Locate and identify every blood parasite.
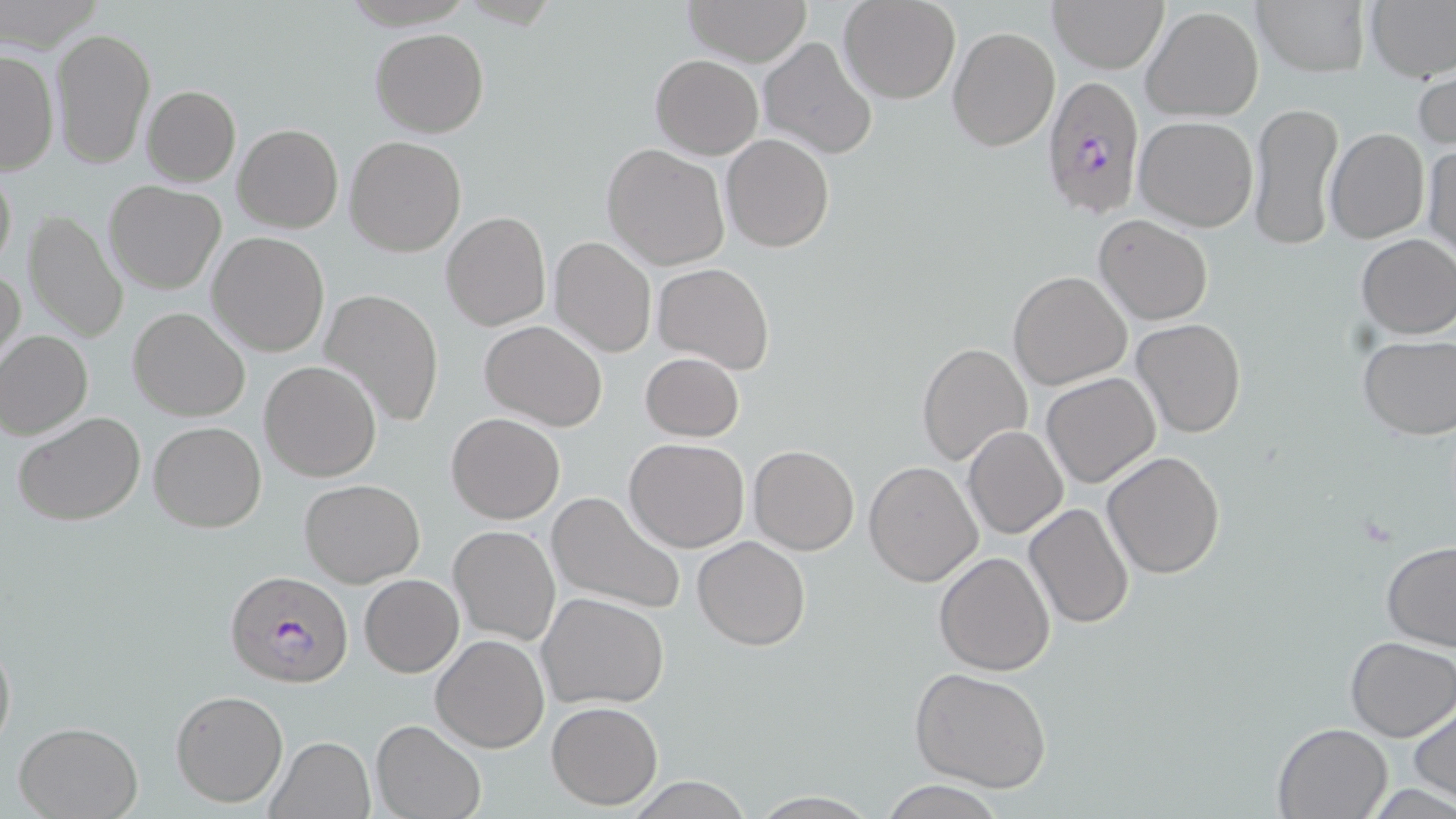

Approximate bounding boxes as named x1/y1/x2/y2 corners in pixels.
Plasmodium falciparum-infected red blood cells: (x1=1039, y1=74, x2=1146, y2=221), (x1=224, y1=568, x2=353, y2=691).
No Plasmodium ovale, Plasmodium malariae, Plasmodium vivax, Babesia divergens, or Trypanosoma brucei observed.

Uninfected red blood cell locations: (x1=3, y1=0, x2=105, y2=52), (x1=684, y1=0, x2=811, y2=65), (x1=838, y1=0, x2=961, y2=103), (x1=1048, y1=0, x2=1168, y2=72), (x1=1250, y1=0, x2=1371, y2=76), (x1=1365, y1=0, x2=1455, y2=81), (x1=1141, y1=5, x2=1264, y2=122), (x1=51, y1=26, x2=156, y2=170), (x1=947, y1=26, x2=1061, y2=151), (x1=371, y1=28, x2=489, y2=137), (x1=758, y1=37, x2=878, y2=160), (x1=0, y1=48, x2=58, y2=174), (x1=651, y1=54, x2=763, y2=158), (x1=1414, y1=64, x2=1455, y2=153), (x1=142, y1=85, x2=241, y2=187), (x1=1248, y1=101, x2=1343, y2=252), (x1=1134, y1=115, x2=1258, y2=232), (x1=233, y1=123, x2=343, y2=233), (x1=1325, y1=128, x2=1429, y2=244), (x1=721, y1=133, x2=834, y2=252), (x1=345, y1=135, x2=468, y2=257), (x1=1422, y1=141, x2=1455, y2=266), (x1=602, y1=143, x2=730, y2=269), (x1=0, y1=160, x2=16, y2=278), (x1=104, y1=180, x2=227, y2=293), (x1=22, y1=209, x2=129, y2=344), (x1=440, y1=210, x2=551, y2=330), (x1=1094, y1=214, x2=1214, y2=325), (x1=208, y1=232, x2=330, y2=357), (x1=1354, y1=233, x2=1456, y2=339), (x1=548, y1=236, x2=657, y2=357), (x1=653, y1=262, x2=775, y2=375), (x1=1, y1=265, x2=25, y2=379), (x1=1007, y1=271, x2=1131, y2=391), (x1=320, y1=287, x2=444, y2=430), (x1=128, y1=307, x2=250, y2=421), (x1=1132, y1=318, x2=1245, y2=438), (x1=479, y1=320, x2=608, y2=431), (x1=0, y1=329, x2=94, y2=440), (x1=1356, y1=333, x2=1455, y2=441), (x1=917, y1=340, x2=1033, y2=469), (x1=640, y1=352, x2=745, y2=442), (x1=260, y1=361, x2=381, y2=481), (x1=1040, y1=372, x2=1160, y2=489), (x1=14, y1=411, x2=147, y2=528), (x1=446, y1=411, x2=566, y2=524), (x1=148, y1=420, x2=266, y2=533), (x1=964, y1=425, x2=1068, y2=540), (x1=623, y1=438, x2=750, y2=553), (x1=748, y1=445, x2=859, y2=555), (x1=1101, y1=450, x2=1226, y2=579), (x1=863, y1=461, x2=983, y2=586), (x1=299, y1=479, x2=425, y2=587), (x1=546, y1=491, x2=686, y2=617), (x1=1023, y1=502, x2=1136, y2=630), (x1=448, y1=525, x2=560, y2=645), (x1=693, y1=536, x2=811, y2=650), (x1=1381, y1=539, x2=1456, y2=651), (x1=934, y1=552, x2=1056, y2=675), (x1=359, y1=575, x2=463, y2=677), (x1=538, y1=592, x2=670, y2=709), (x1=0, y1=624, x2=15, y2=758), (x1=431, y1=635, x2=549, y2=752), (x1=1344, y1=636, x2=1455, y2=741), (x1=910, y1=667, x2=1055, y2=792), (x1=169, y1=689, x2=288, y2=808), (x1=1410, y1=698, x2=1455, y2=805), (x1=547, y1=701, x2=662, y2=810), (x1=371, y1=719, x2=486, y2=819), (x1=13, y1=721, x2=144, y2=819), (x1=1273, y1=721, x2=1393, y2=817), (x1=266, y1=736, x2=377, y2=819), (x1=620, y1=778, x2=759, y2=817), (x1=876, y1=779, x2=1006, y2=818). Slide-level diagnosis: Plasmodium falciparum. Thin blood smear. Optical microscopy. Image is 1456×819 pixels. May-Grünwald-Giemsa stain. Captured at 1000x magnification. Single field of view.